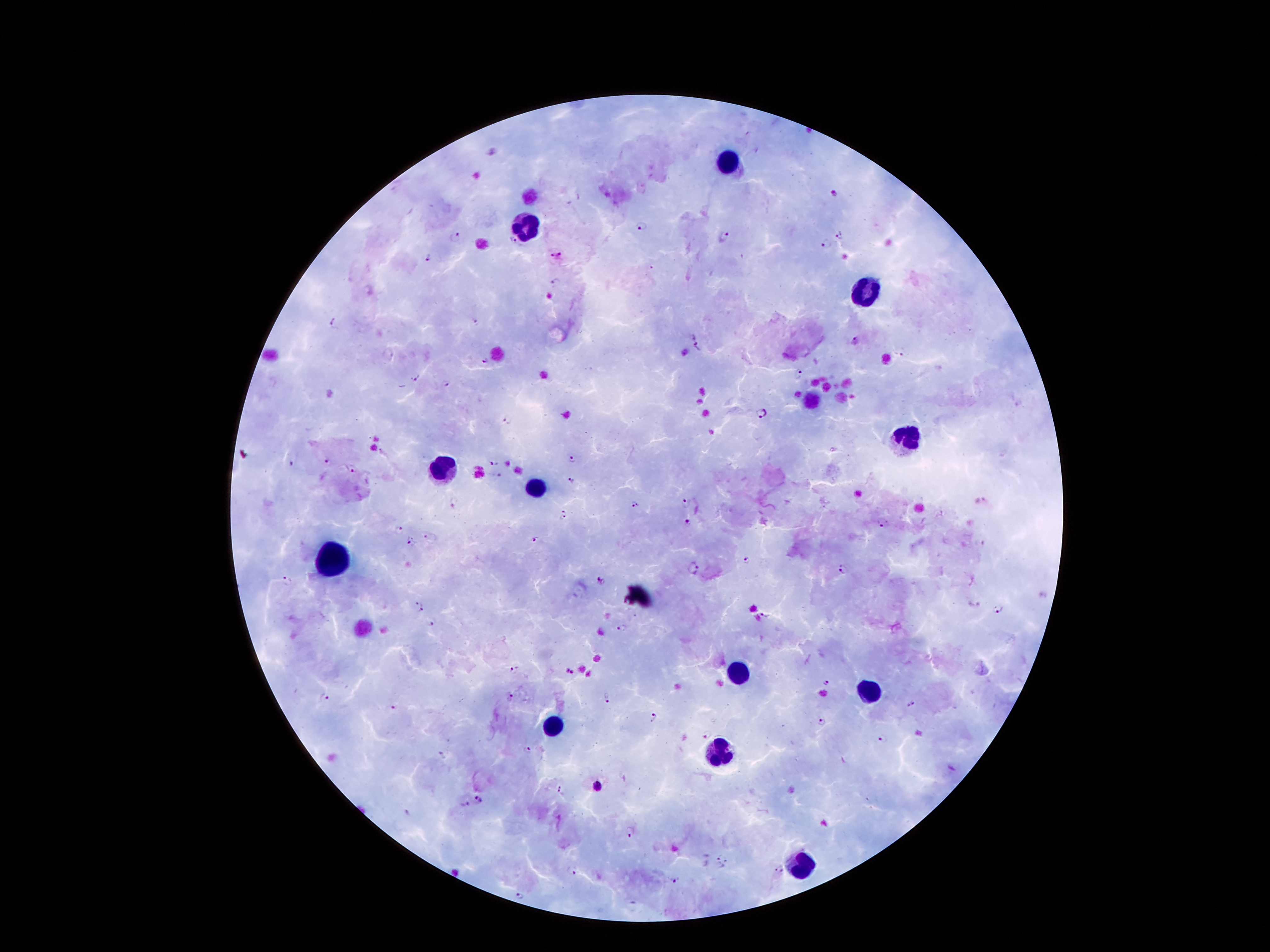
preparation: thick peripheral-blood smear
stain: Giemsa
image_size: 1270×952 pixels
patient_malaria_status: infected with Plasmodium falciparum
capture: smartphone through the microscope eyepiece
leukocyte_locations: 'approximate object centers, in pixels from the top-left corner: (x=731, y=162), (x=530, y=223), (x=866, y=290), (x=909, y=437), (x=442, y=466), (x=536, y=486), (x=330, y=559), (x=734, y=674), (x=869, y=694), (x=556, y=725), (x=718, y=753), (x=802, y=865)'
magnification: 100x
field_of_view: single
plasmodium_parasite_locations: 'approximate object centers, in pixels from the top-left corner: (x=832, y=192), (x=640, y=227), (x=454, y=236), (x=842, y=237), (x=723, y=239), (x=512, y=243), (x=826, y=245), (x=427, y=256), (x=557, y=256), (x=555, y=282), (x=476, y=321), (x=333, y=322), (x=856, y=340), (x=698, y=345), (x=903, y=354), (x=484, y=360), (x=800, y=373), (x=414, y=377), (x=447, y=383), (x=762, y=413), (x=508, y=419), (x=571, y=459), (x=327, y=461), (x=493, y=462), (x=290, y=464), (x=354, y=469), (x=500, y=475), (x=570, y=480), (x=454, y=500), (x=634, y=504), (x=684, y=504), (x=567, y=514), (x=883, y=523), (x=687, y=524), (x=398, y=531), (x=428, y=537), (x=535, y=540), (x=409, y=541), (x=744, y=560), (x=696, y=567), (x=842, y=569), (x=286, y=581), (x=599, y=581), (x=415, y=604), (x=972, y=605), (x=997, y=605), (x=422, y=609), (x=767, y=613), (x=434, y=624), (x=622, y=626), (x=515, y=670), (x=570, y=672), (x=826, y=682), (x=512, y=697), (x=325, y=698), (x=608, y=698), (x=911, y=704), (x=393, y=707), (x=654, y=718), (x=822, y=721), (x=707, y=735), (x=879, y=737), (x=528, y=751), (x=597, y=788), (x=560, y=790), (x=479, y=799), (x=466, y=804), (x=632, y=832), (x=722, y=860), (x=570, y=870), (x=778, y=870), (x=674, y=879), (x=519, y=896)'